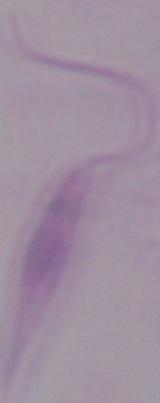

Summary:
  - Modality: photomicrograph
  - Magnification: 1000x
  - Identification: Leishmania